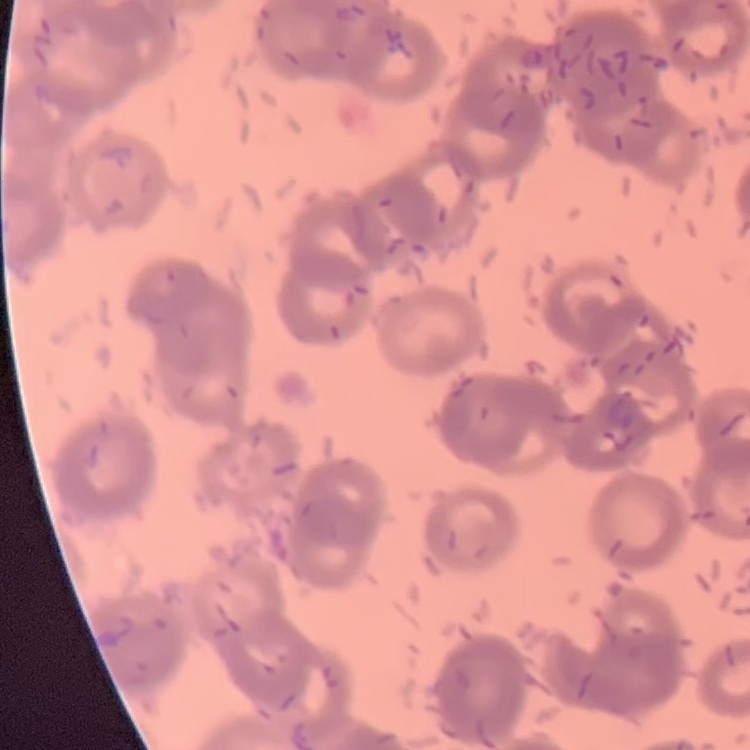

The erythrocytes exhibit rouleaux formation. Stained with either Field's or Giemsa. Thin peripheral smear. One tile cut from a larger photomicrograph.